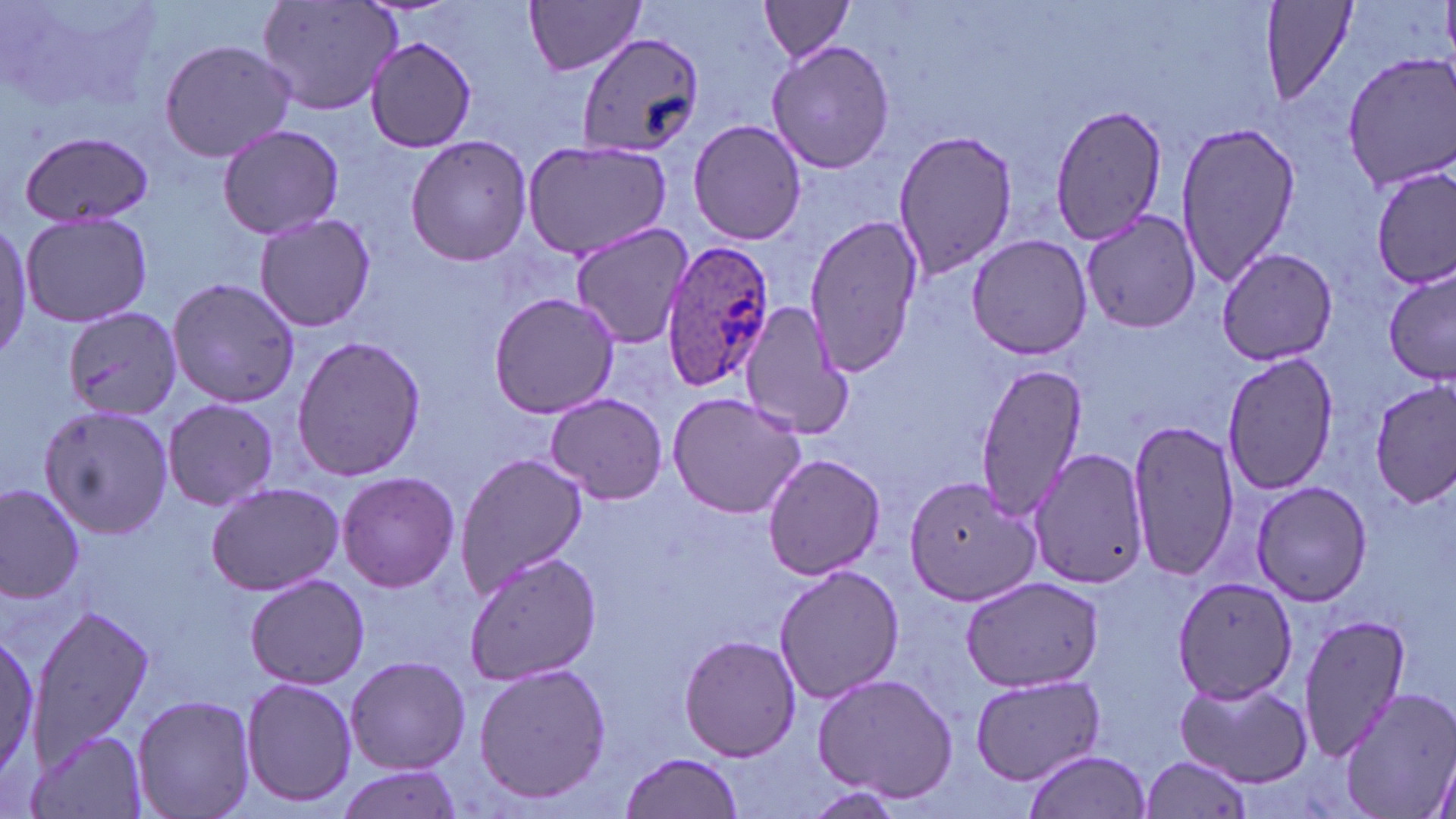

Plasmodium ovale-infected red blood cell locations = approximate bounding boxes as (x1,y1)-(x2,y2) corner pairs in pixels: (658,239)-(773,391)
slide-level diagnosis = Plasmodium ovale
magnification = 1000x
field of view = single
stain = May-Grünwald-Giemsa
preparation = thin blood smear
modality = optical microscopy
uninfected red blood cell locations = approximate bounding boxes as (x1,y1)-(x2,y2) corner pairs in pixels: (257,0)-(402,117), (524,0)-(646,77), (1258,0)-(1359,113), (757,1)-(857,62), (576,30)-(703,159), (159,34)-(300,165), (361,34)-(481,152), (766,40)-(896,174), (1340,52)-(1456,193), (1045,102)-(1170,247), (687,118)-(809,246), (1174,120)-(1301,288), (216,124)-(344,240), (893,127)-(1020,279), (13,128)-(154,228), (405,134)-(533,267), (521,141)-(673,260), (1372,167)-(1453,289), (1080,208)-(1203,334), (20,210)-(154,328), (252,211)-(377,334), (802,214)-(922,379), (0,221)-(33,359), (569,221)-(696,350), (966,234)-(1094,359), (1213,247)-(1342,366), (1382,269)-(1456,385), (166,279)-(302,409), (488,291)-(623,420), (738,301)-(851,442), (63,306)-(183,424), (291,335)-(426,480), (1221,353)-(1340,494), (973,361)-(1091,520), (1370,382)-(1454,507), (667,389)-(809,519), (545,393)-(667,503), (161,398)-(282,512), (35,403)-(175,539), (1128,419)-(1239,582), (1026,445)-(1152,591), (455,453)-(589,597), (761,453)-(885,580), (335,470)-(461,593), (905,474)-(1039,607), (1249,481)-(1375,607), (0,482)-(88,603), (206,482)-(343,596), (463,550)-(601,687), (773,564)-(907,705), (244,573)-(371,689), (959,576)-(1106,692), (1170,576)-(1299,703), (29,603)-(151,767), (1297,614)-(1413,763), (0,619)-(47,795), (680,634)-(802,761), (343,654)-(471,774), (470,661)-(614,806), (811,671)-(959,802), (971,673)-(1104,785), (238,676)-(358,810), (1174,677)-(1314,787), (1332,686)-(1456,819), (130,694)-(257,819), (29,731)-(148,818), (617,751)-(746,819), (1022,751)-(1150,819), (1139,755)-(1254,819), (331,764)-(468,819)
image size = 1456×819 pixels